Locate and identify every blood parasite.
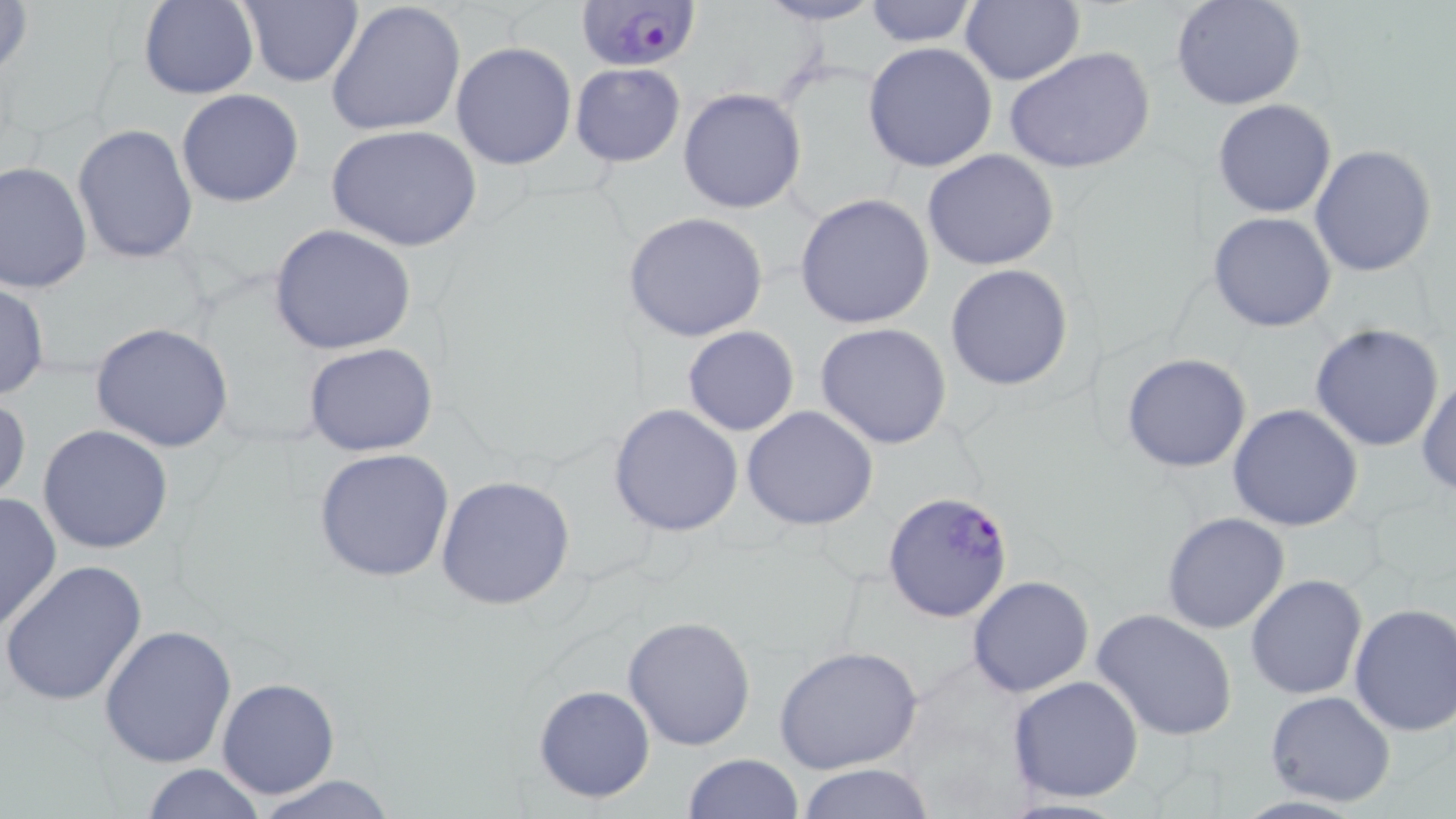

Approximate bounding boxes as named x1/y1/x2/y2 corners in pixels.
Plasmodium falciparum-infected red blood cells: (x1=573, y1=0, x2=699, y2=72), (x1=881, y1=490, x2=1015, y2=622).
No Plasmodium ovale, Plasmodium malariae, Plasmodium vivax, Babesia divergens, or Trypanosoma brucei observed.

slide-level diagnosis = Plasmodium falciparum
field of view = single
magnification = 1000x
uninfected red blood cell locations = approximate bounding boxes as named x1/y1/x2/y2 corners in pixels: (x1=1, y1=0, x2=32, y2=84), (x1=325, y1=0, x2=465, y2=139), (x1=961, y1=0, x2=1084, y2=87), (x1=1171, y1=0, x2=1307, y2=111), (x1=139, y1=1, x2=258, y2=99), (x1=754, y1=1, x2=886, y2=26), (x1=861, y1=1, x2=981, y2=48), (x1=236, y1=2, x2=363, y2=87), (x1=864, y1=41, x2=999, y2=173), (x1=450, y1=42, x2=578, y2=171), (x1=1004, y1=47, x2=1156, y2=176), (x1=569, y1=62, x2=686, y2=167), (x1=677, y1=88, x2=806, y2=213), (x1=176, y1=89, x2=304, y2=208), (x1=1213, y1=99, x2=1337, y2=218), (x1=325, y1=123, x2=484, y2=251), (x1=73, y1=124, x2=198, y2=266), (x1=1310, y1=145, x2=1438, y2=279), (x1=920, y1=149, x2=1061, y2=272), (x1=0, y1=159, x2=92, y2=294), (x1=794, y1=193, x2=936, y2=328), (x1=1208, y1=211, x2=1338, y2=332), (x1=624, y1=212, x2=770, y2=341), (x1=271, y1=225, x2=416, y2=356), (x1=945, y1=263, x2=1073, y2=391), (x1=0, y1=281, x2=49, y2=401), (x1=90, y1=322, x2=235, y2=452), (x1=1310, y1=322, x2=1444, y2=450), (x1=814, y1=323, x2=954, y2=449), (x1=682, y1=326, x2=799, y2=436), (x1=303, y1=343, x2=439, y2=457), (x1=1121, y1=352, x2=1252, y2=474), (x1=1417, y1=372, x2=1455, y2=496), (x1=1, y1=390, x2=31, y2=509), (x1=610, y1=402, x2=744, y2=537), (x1=1228, y1=403, x2=1364, y2=533), (x1=740, y1=406, x2=880, y2=532), (x1=38, y1=423, x2=174, y2=555), (x1=312, y1=448, x2=455, y2=582), (x1=436, y1=475, x2=576, y2=612), (x1=0, y1=490, x2=62, y2=634), (x1=1160, y1=512, x2=1290, y2=635), (x1=1, y1=560, x2=149, y2=708), (x1=1245, y1=574, x2=1367, y2=701), (x1=967, y1=575, x2=1094, y2=697), (x1=1348, y1=601, x2=1456, y2=739), (x1=1092, y1=608, x2=1237, y2=743), (x1=622, y1=615, x2=757, y2=751), (x1=99, y1=624, x2=237, y2=768), (x1=774, y1=644, x2=923, y2=775), (x1=1007, y1=674, x2=1144, y2=803), (x1=216, y1=677, x2=340, y2=800), (x1=531, y1=683, x2=657, y2=804), (x1=1266, y1=690, x2=1397, y2=807), (x1=682, y1=753, x2=802, y2=819), (x1=139, y1=763, x2=264, y2=819), (x1=794, y1=763, x2=939, y2=818), (x1=248, y1=775, x2=403, y2=819)
image size = 1456×819 pixels
stain = May-Grünwald-Giemsa
preparation = thin blood film
modality = light microscopy